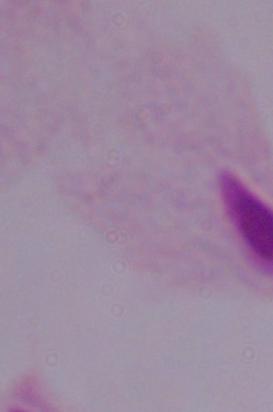

A trichomonad is shown. Photomicrograph. Captured at 1000x magnification.